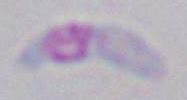

modality: photomicrograph
identification: Toxoplasma gondii
magnification: 1000x